Report the malaria status of this cell.
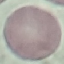
It is uninfected.

preparation: thin blood film
capture: smartphone camera at the microscope eyepiece
stain: Giemsa
image_type: cell patch, automatically extracted from a larger field of view and resized to 64 × 64 pixels